Mark where platelets are.
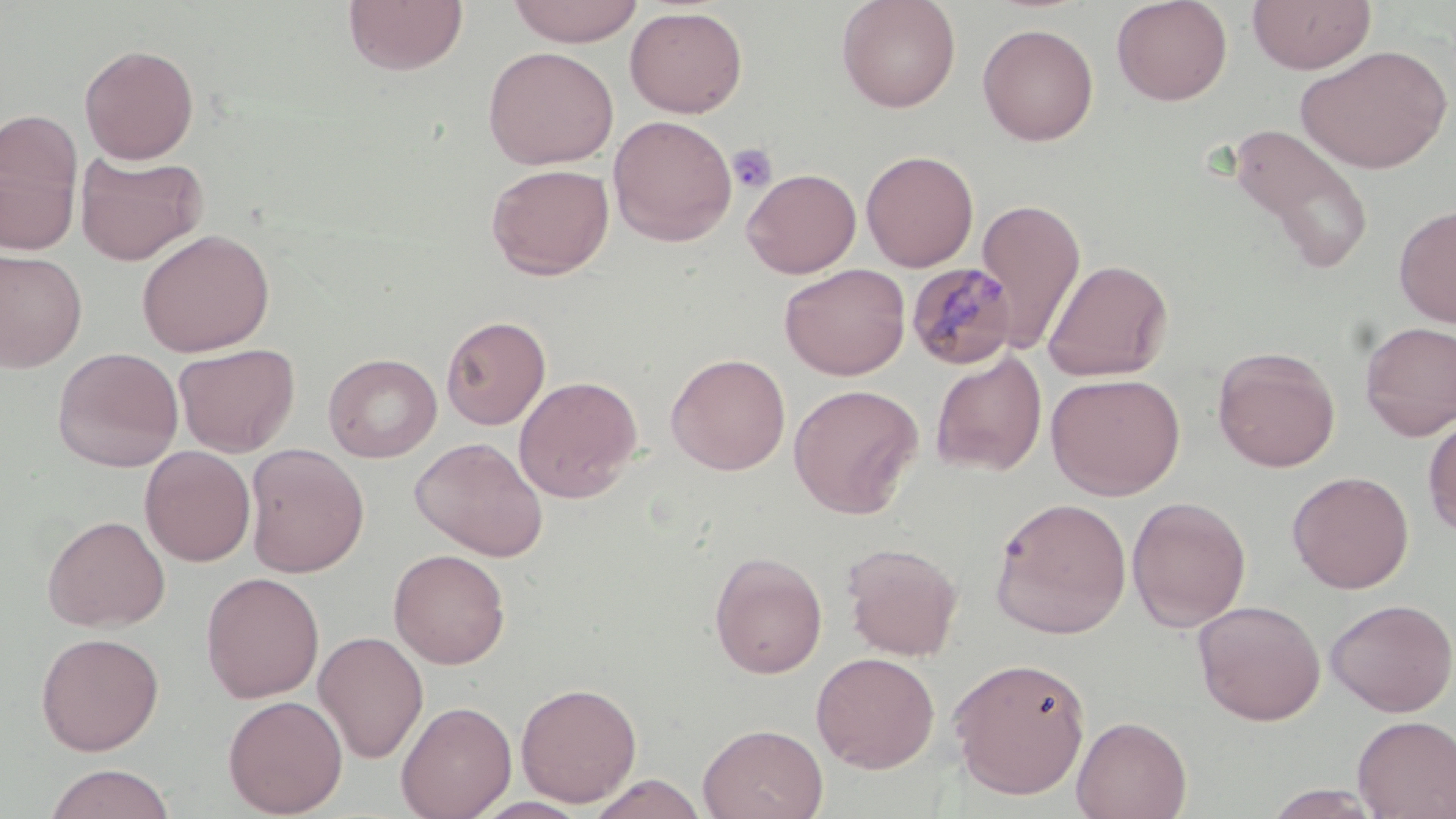

Approximate bounding boxes as (x1,y1)-(x2,y2) corner pairs in pixels.
Platelets: (728,144)-(778,194).

Summary:
  - Plasmodium malariae-infected red blood cell locations: (906,262)-(1018,371)
  - Uninfected red blood cell locations: (343,0)-(469,76), (506,0)-(645,46), (836,0)-(961,113), (1111,0)-(1233,106), (1247,0)-(1376,73), (625,6)-(748,118), (977,22)-(1098,146), (79,43)-(200,164), (1295,44)-(1453,174), (482,45)-(619,170), (0,112)-(83,254), (608,114)-(737,246), (1226,123)-(1375,278), (861,150)-(978,272), (75,152)-(207,266), (486,163)-(615,280), (741,167)-(862,278), (975,197)-(1087,352), (1394,204)-(1456,327), (136,228)-(275,357), (0,249)-(88,372), (1043,258)-(1173,381), (779,263)-(911,380), (441,315)-(551,430), (1358,320)-(1456,440), (173,343)-(300,457), (1213,346)-(1341,473), (52,347)-(184,472), (323,352)-(442,463), (665,352)-(791,475), (930,352)-(1047,476), (1046,372)-(1185,500), (513,375)-(643,503), (787,384)-(923,518), (1423,413)-(1456,537), (410,436)-(548,561), (244,443)-(369,578), (139,445)-(256,566), (1287,470)-(1414,594), (1127,496)-(1251,632), (989,497)-(1132,639), (42,514)-(171,632), (841,541)-(963,660), (832,543)-(951,776), (388,549)-(511,669), (709,551)-(827,678), (201,571)-(325,703), (1325,598)-(1456,717), (1193,599)-(1325,725), (313,631)-(429,764), (36,632)-(165,755), (811,651)-(940,773), (948,656)-(1091,800), (515,681)-(642,807), (222,694)-(348,817), (396,700)-(517,819), (1072,715)-(1192,819), (1352,715)-(1456,819), (697,723)-(828,819), (43,764)-(177,819), (588,773)-(707,819), (1261,785)-(1388,819)
  - Slide-level diagnosis: Plasmodium malariae
  - Preparation: thin blood film
  - Image size: 1456×819 pixels
  - Modality: optical microscopy
  - Magnification: 1000x
  - Stain: May-Grünwald-Giemsa
  - Field of view: single